Classify this cell by malaria status.
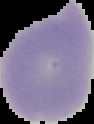
Uninfected.

image type = cell region segmented out of the field of view; surrounding area masked to black
image size = 94×124 pixels
preparation = thin blood film